Evaluate for malaria.
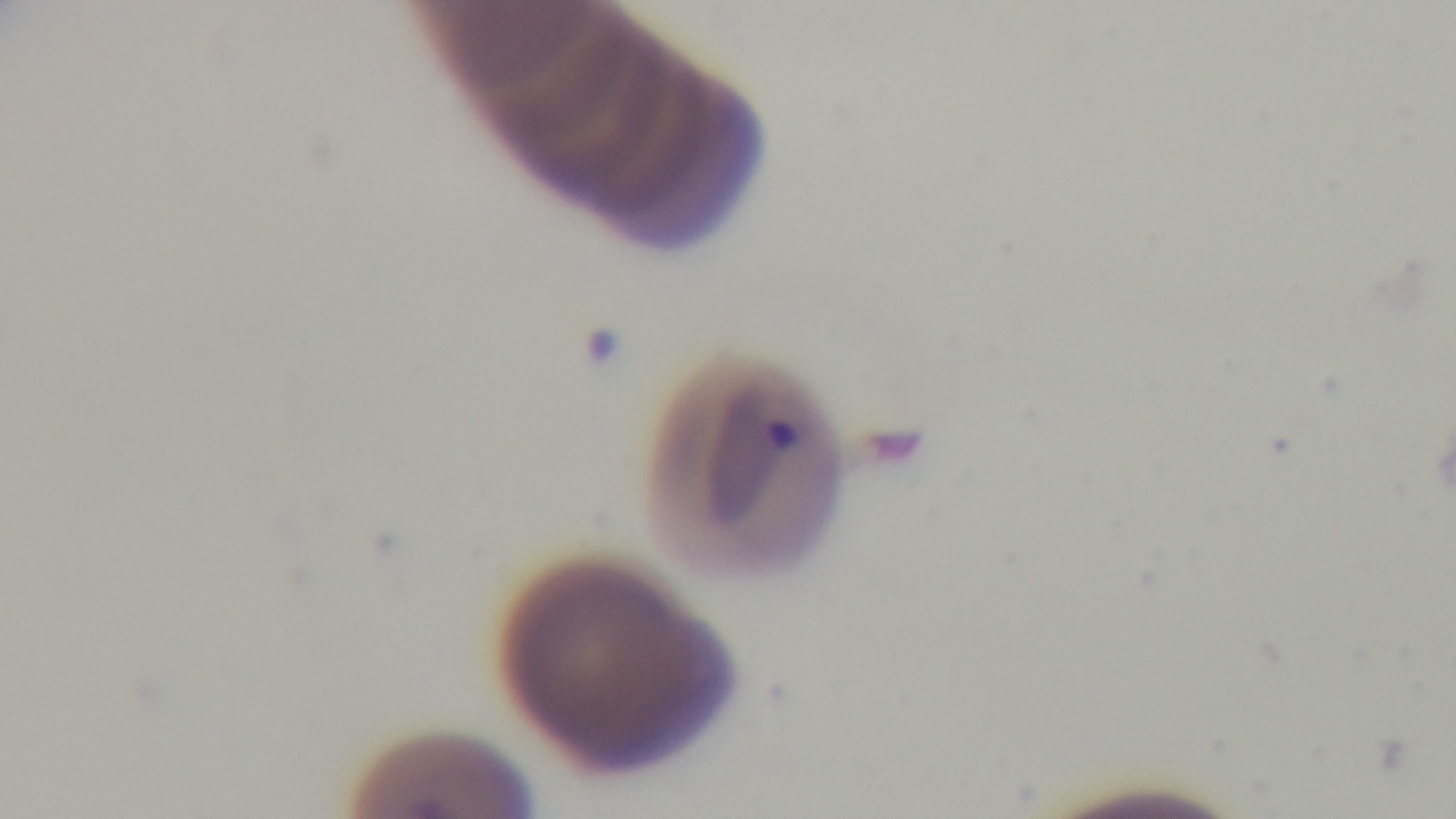
Infected.

stain = Giemsa
field of view = one from the slide
objective = 100x oil immersion
modality = light microscopy
preparation = thin
capture = mounted 4K digital camera